Give the extent of all uninfected red blood cells.
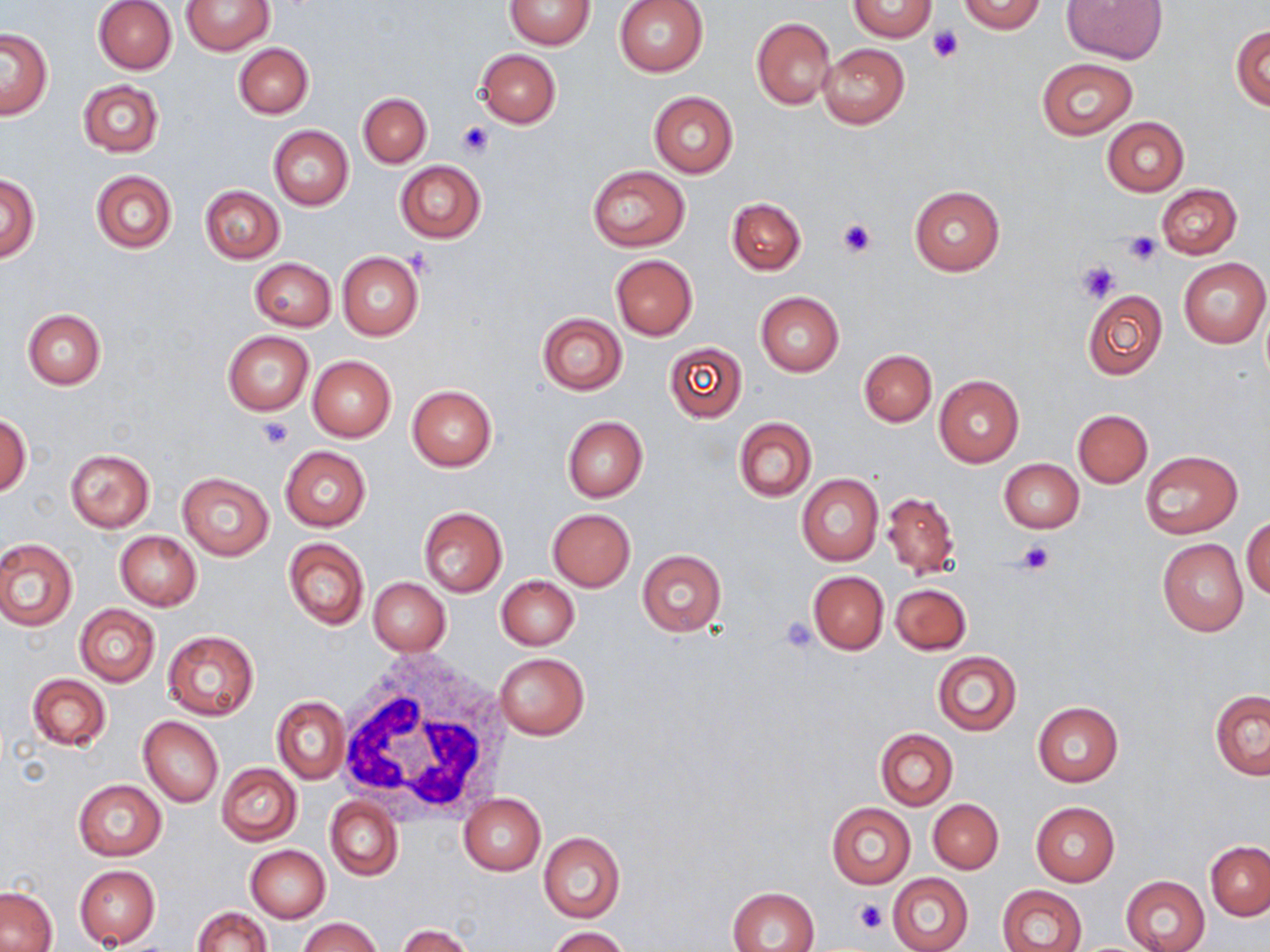

Approximate bounding boxes as [x1, y1, x2, y2] in pixels.
Uninfected red blood cells: [93, 0, 176, 74], [613, 0, 709, 77], [848, 0, 935, 40], [958, 0, 1045, 34], [1062, 0, 1167, 64], [181, 1, 275, 55], [505, 1, 596, 49], [751, 19, 836, 109], [1231, 26, 1270, 111], [1, 29, 51, 117], [234, 43, 313, 119], [819, 43, 910, 129], [475, 49, 560, 128], [1035, 57, 1138, 138], [77, 79, 164, 156], [648, 90, 739, 178], [358, 93, 431, 166], [1102, 116, 1189, 195], [268, 124, 354, 210], [395, 161, 485, 243], [587, 165, 690, 251], [90, 170, 177, 253], [1, 174, 39, 261], [908, 184, 1005, 277], [1156, 184, 1242, 258], [200, 186, 284, 262], [727, 197, 806, 276], [337, 251, 424, 341], [610, 255, 698, 339], [249, 257, 336, 331], [1179, 258, 1269, 347], [1082, 290, 1168, 379], [754, 292, 843, 377], [1261, 302, 1270, 384], [22, 308, 106, 388], [538, 313, 626, 395], [222, 331, 314, 415], [663, 342, 747, 422], [858, 348, 936, 426], [307, 355, 396, 442], [934, 373, 1025, 468], [406, 385, 496, 472], [1073, 409, 1152, 487], [1, 415, 31, 495], [562, 416, 647, 502], [733, 417, 817, 501], [280, 446, 371, 531], [65, 448, 155, 531], [1141, 450, 1241, 538], [999, 459, 1084, 533], [178, 471, 274, 561], [796, 473, 883, 566], [883, 492, 958, 580], [418, 506, 507, 597], [547, 509, 636, 591], [1244, 515, 1270, 600], [116, 531, 199, 610], [0, 537, 78, 631], [283, 537, 368, 630], [1158, 538, 1248, 637], [636, 550, 728, 636], [806, 570, 889, 656], [497, 576, 579, 650], [369, 577, 451, 656], [891, 582, 971, 655], [74, 604, 160, 686], [163, 631, 259, 721], [932, 651, 1022, 736], [495, 653, 589, 739], [28, 672, 111, 751], [1210, 690, 1270, 780], [273, 696, 349, 783], [1033, 702, 1122, 786], [139, 716, 223, 808], [875, 728, 957, 810], [216, 763, 302, 845], [73, 779, 167, 860], [459, 794, 546, 875], [325, 797, 402, 881], [928, 798, 1004, 873], [1031, 802, 1119, 886], [825, 803, 915, 889], [538, 832, 625, 923], [1206, 842, 1270, 920], [246, 846, 330, 923], [74, 865, 160, 948], [887, 873, 974, 952], [1120, 874, 1210, 952], [996, 885, 1087, 952], [1, 887, 57, 952], [728, 887, 820, 952], [193, 907, 270, 952], [298, 917, 383, 952], [396, 925, 474, 952], [547, 927, 629, 951].

Platelet locations: [929, 26, 963, 62], [455, 121, 495, 158], [836, 217, 877, 260], [1123, 231, 1161, 267], [406, 250, 435, 278], [1077, 260, 1119, 304], [256, 415, 293, 449], [1017, 540, 1053, 575], [779, 617, 817, 653], [854, 898, 887, 935]. White blood cell locations: [333, 650, 515, 826]. Slide-level diagnosis: negative for blood parasites. Image is 1270×952 pixels. Captured at 1000x magnification. Thin blood film. May-Grünwald-Giemsa-stained preparation. One field of a larger specimen. Light microscopy.